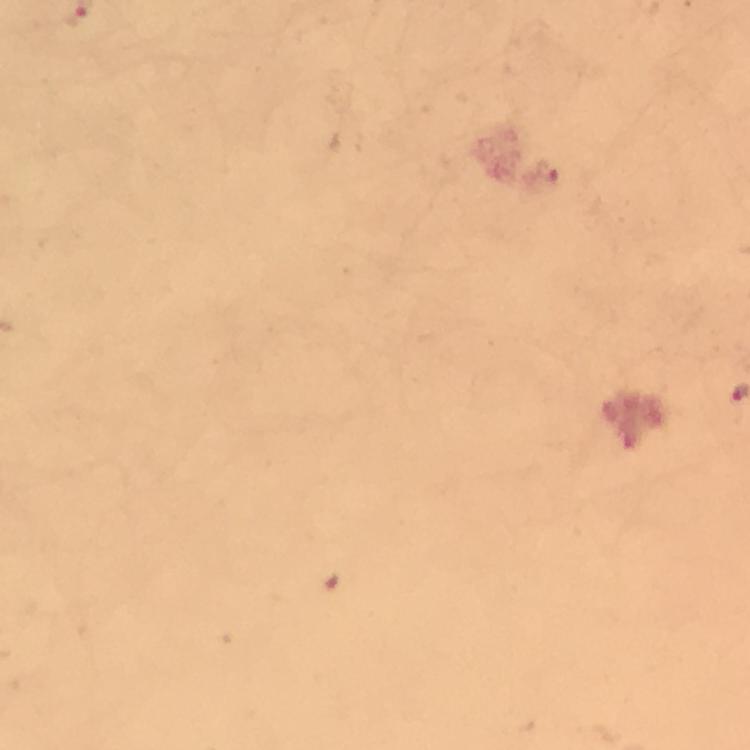
capture: smartphone mounted on the microscope
immersion_oil: used
malaria_parasite_locations: 'approximate centers as {x, y} in pixels: {546, 172}'
magnification: 100x
image_size: 750×750 pixels
cropped_from: a single field of view
preparation: thick blood smear
stain: Giemsa
context: from a malaria diagnostic workup